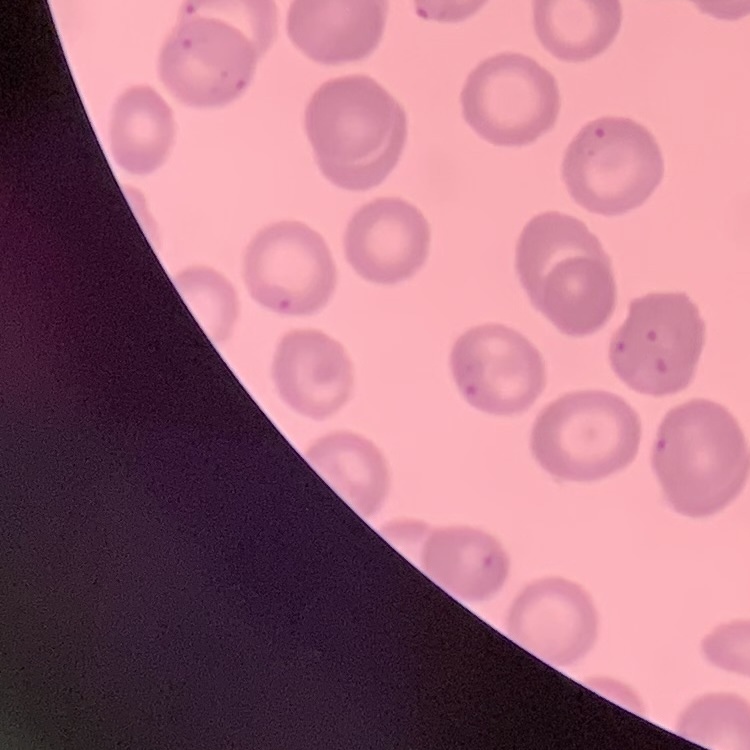

The red blood cells exhibit no rouleaux formation. Thin peripheral smear. One tile cut from a larger photomicrograph. Field's or Giemsa stain.